Classify this cell by malaria status.
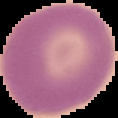
Uninfected.

preparation = thin blood film
image size = 118×118 pixels
image type = segmented cell region with the area outside set to black